Locate every blood parasite and identify its species.
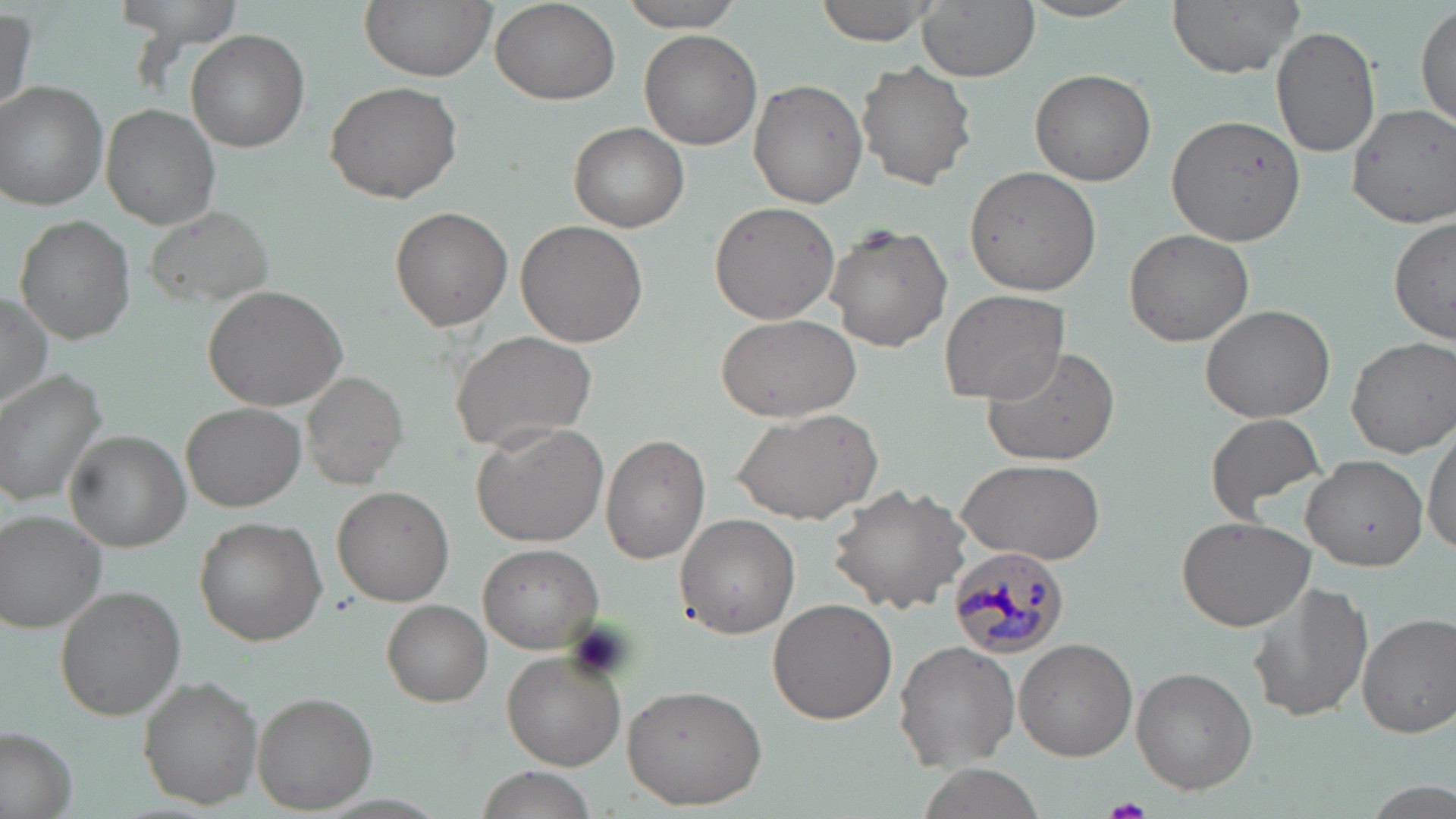
Approximate bounding boxes as (x1, y1, x2, y2) in pixels.
Plasmodium malariae-infected red blood cells: (949, 546, 1073, 658).
No Plasmodium falciparum, Plasmodium ovale, Plasmodium vivax, Babesia divergens, or Trypanosoma brucei observed.

slide-level diagnosis = Plasmodium malariae
platelet locations = approximate bounding boxes as (x1, y1, x2, y2) in pixels: (1103, 799, 1155, 819)
preparation = thin blood film
stain = May-Grünwald-Giemsa
uninfected red blood cell locations = approximate bounding boxes as (x1, y1, x2, y2) in pixels: (112, 0, 248, 46), (360, 0, 496, 81), (812, 0, 948, 46), (914, 0, 1038, 80), (1167, 0, 1306, 77), (1018, 1, 1148, 24), (490, 2, 619, 107), (615, 2, 750, 31), (1414, 3, 1455, 128), (1, 7, 35, 118), (1270, 24, 1379, 158), (186, 30, 309, 152), (639, 30, 762, 150), (856, 62, 978, 190), (1029, 67, 1157, 187), (747, 78, 867, 209), (325, 79, 465, 205), (0, 82, 110, 210), (1343, 102, 1456, 229), (100, 104, 220, 228), (1165, 113, 1307, 249), (568, 122, 691, 232), (966, 164, 1101, 295), (708, 201, 841, 324), (145, 205, 270, 307), (390, 208, 512, 331), (1389, 214, 1454, 345), (15, 215, 136, 343), (516, 220, 648, 348), (826, 222, 952, 353), (1124, 228, 1252, 347), (204, 284, 348, 410), (939, 288, 1071, 404), (0, 293, 52, 413), (1200, 303, 1336, 424), (714, 313, 860, 419), (448, 329, 597, 455), (1346, 336, 1456, 458), (982, 344, 1121, 469), (0, 371, 107, 506), (299, 371, 405, 488), (181, 402, 305, 510), (733, 405, 882, 527), (1204, 412, 1329, 523), (471, 421, 609, 548), (1423, 424, 1455, 557), (64, 431, 190, 550), (601, 434, 711, 563), (1302, 453, 1427, 571), (956, 457, 1107, 564), (829, 481, 973, 613), (332, 486, 453, 605), (0, 509, 107, 635), (675, 514, 800, 639), (1174, 515, 1316, 634), (195, 517, 327, 647), (477, 543, 602, 653), (1246, 577, 1375, 726), (58, 586, 185, 719), (767, 599, 896, 724), (380, 600, 493, 706), (1356, 613, 1456, 737), (1013, 638, 1137, 761), (894, 642, 1020, 771), (501, 649, 626, 768), (1131, 665, 1257, 792), (139, 677, 263, 809), (620, 683, 768, 810), (253, 688, 380, 814), (1, 729, 77, 817), (474, 766, 604, 819)
field of view = single
modality = optical microscopy
magnification = 1000x
image size = 1456×819 pixels